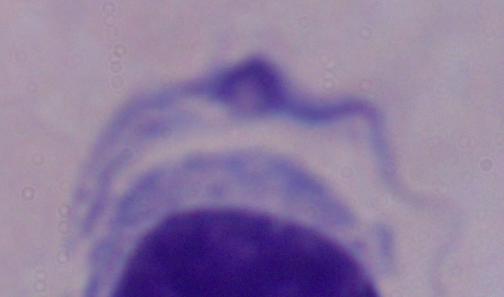
Captured at 1000x magnification. A trypanosome is shown. Photomicrograph.